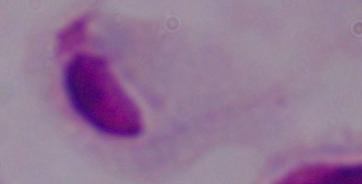
modality = micrograph
magnification = 1000x
identification = trichomonad